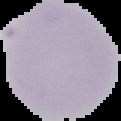

preparation = thin blood smear
image size = 121×121 pixels
image type = segmented cell region on a black background
malaria status = uninfected